Identify the parasite.
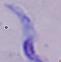
A trypanosome.

Micrograph. Captured at 1000x magnification.